Assess this cell for malaria.
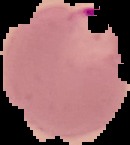
Parasitized.

Image is 130×145 pixels. From a thin blood smear. Segmented cell region on a black background.